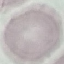 Result: no malaria parasites seen. Thin blood film. Photographed with a smartphone camera at the microscope eyepiece. Cell patch, automatically extracted from a larger field of view and resized to 64 × 64 pixels. Giemsa stain.